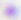

Summary:
  - Magnification: 400x
  - Identification: Toxoplasma gondii
  - Modality: micrograph